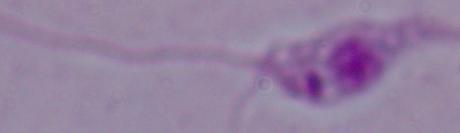
Micrograph. Captured at 1000x magnification. A Leishmania parasite is shown.